Give the position of every Plasmodium parasite visible.
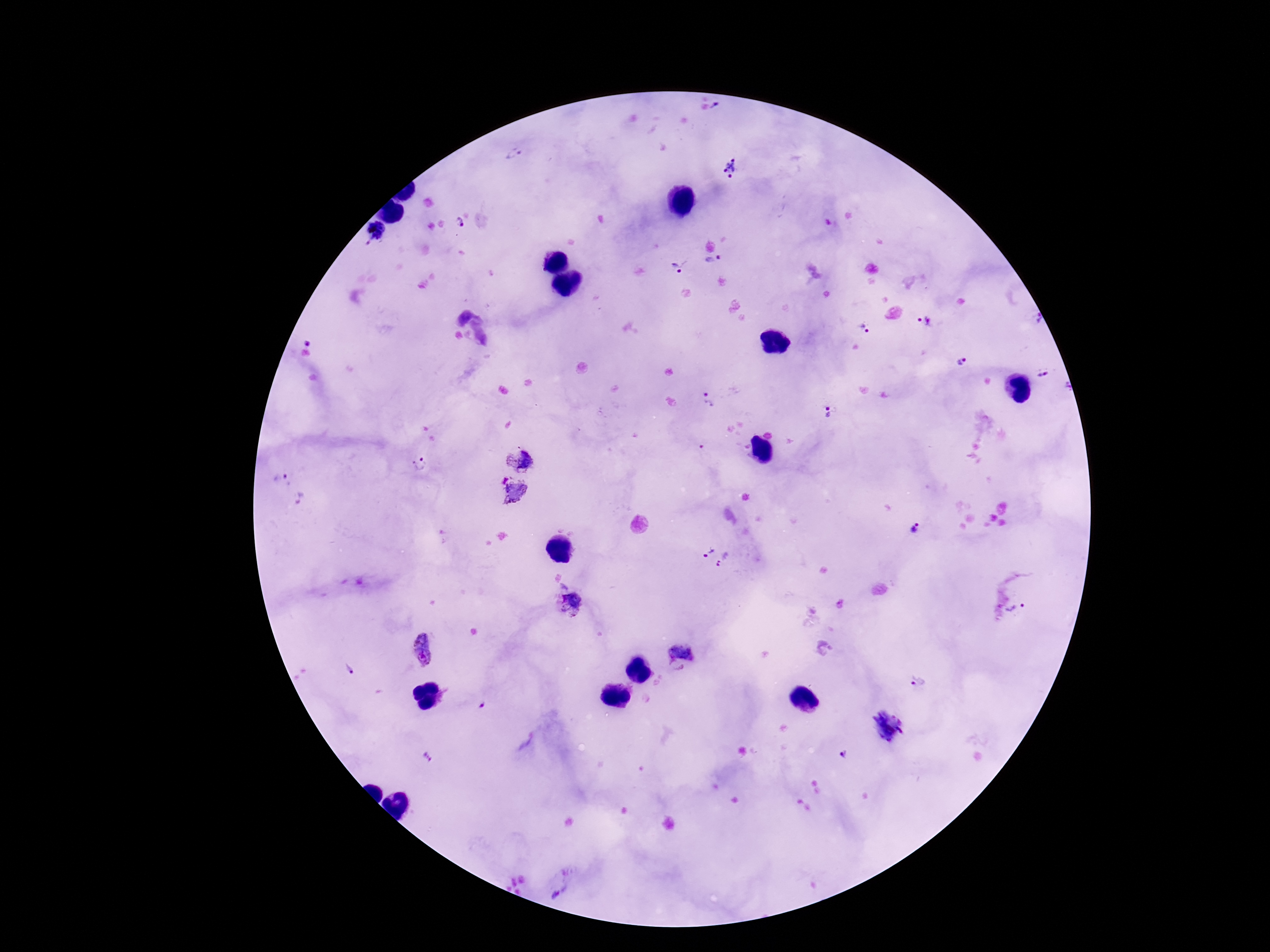

Approximate centers as [x, y] in pixels.
Plasmodium parasites: [513, 155], [731, 168], [461, 223], [375, 233], [714, 262], [680, 265], [925, 321], [863, 328], [306, 339], [962, 360], [1042, 374], [710, 400], [827, 413], [520, 457], [421, 463], [280, 479], [513, 493], [301, 500], [914, 530], [708, 552], [724, 560], [571, 605], [1016, 610], [422, 631], [683, 651], [423, 659], [350, 668], [915, 683], [482, 704], [890, 726], [843, 754], [429, 756], [560, 893].

Smartphone photograph taken through the microscope eyepiece. Single field of view. 100x magnification. Giemsa-stained preparation. Image is 1270×952 pixels. Patient malaria status: infected. Thick blood smear.